State which cell type is depicted.
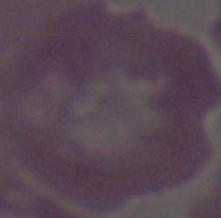

This is an erythrocyte.

Summary:
  - Modality: photomicrograph
  - Magnification: 1000x